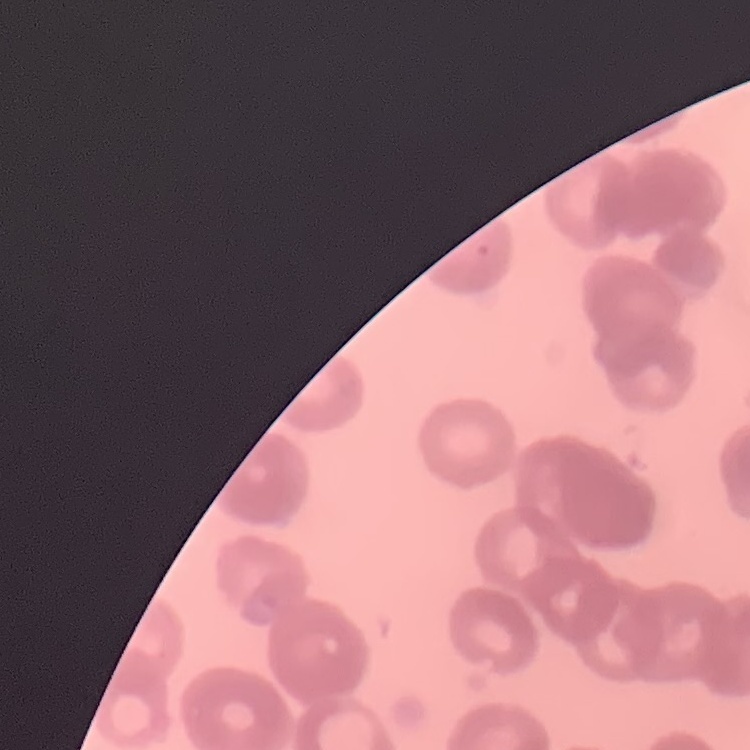
Summary:
  - Red blood cell morphology: rouleaux formation
  - Preparation: thin blood film
  - Stain: Field's or Giemsa
  - Image type: one tile cut from a larger photomicrograph